Locate every uninfected red blood cell.
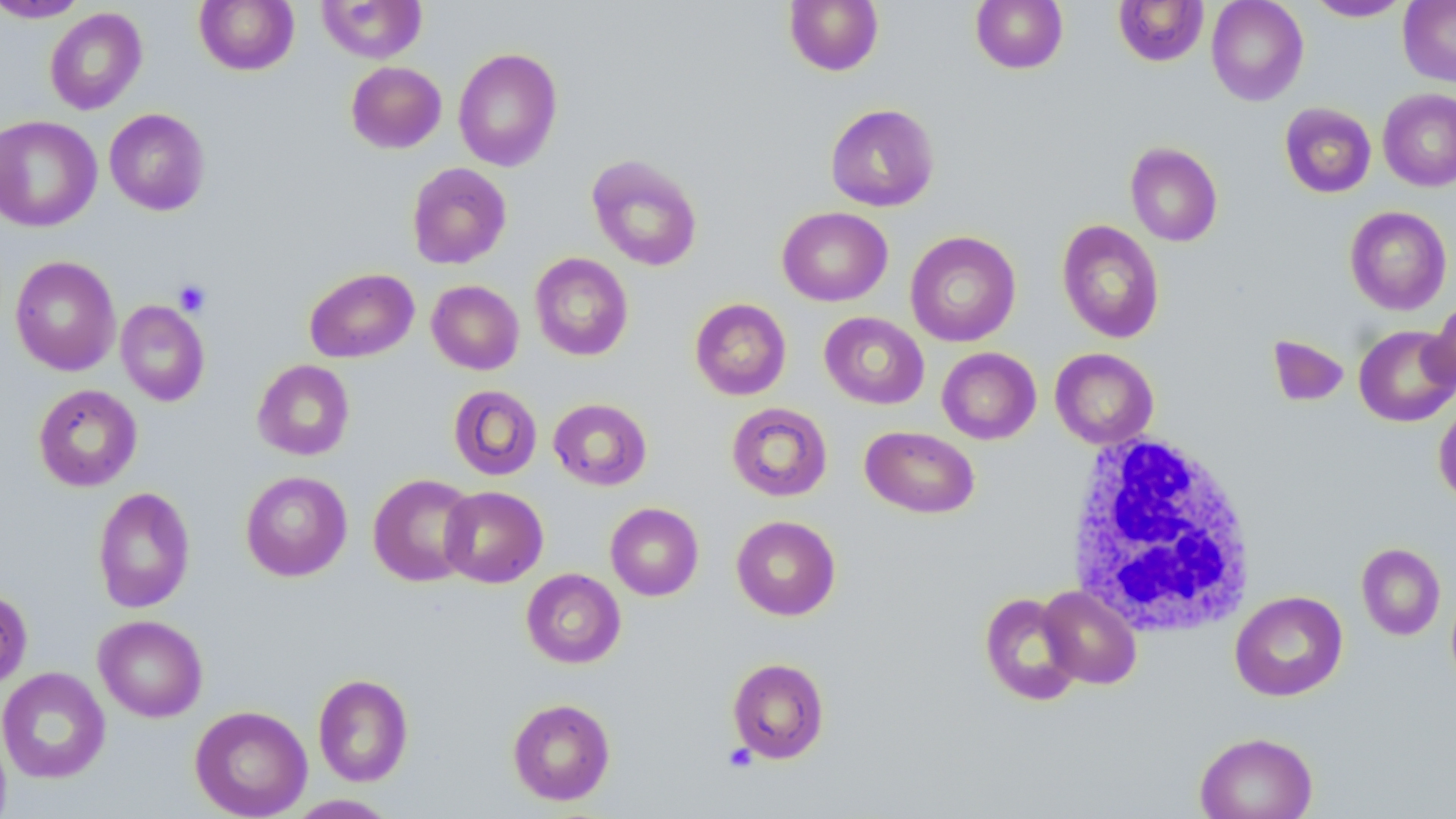
Approximate bounding boxes as (x1,y1)-(x2,y2) corner pairs in pixels.
Uninfected red blood cells: (0,0)-(90,23), (194,0)-(299,75), (783,0)-(884,76), (970,0)-(1068,74), (1113,0)-(1209,67), (1206,0)-(1309,106), (1304,0)-(1412,22), (316,1)-(427,63), (1399,1)-(1456,86), (44,7)-(148,115), (453,47)-(563,171), (345,61)-(447,153), (1378,88)-(1456,191), (1280,102)-(1376,198), (825,103)-(940,212), (104,108)-(211,215), (0,115)-(102,232), (1125,142)-(1223,246), (587,153)-(703,272), (406,162)-(512,269), (1344,205)-(1452,315), (777,206)-(892,306), (1057,220)-(1165,344), (905,231)-(1021,346), (530,253)-(633,361), (9,255)-(121,376), (304,268)-(419,363), (427,280)-(524,375), (689,298)-(792,400), (116,299)-(210,406), (1424,300)-(1456,397), (819,312)-(929,409), (1353,324)-(1456,427), (1268,334)-(1454,410), (1268,335)-(1350,407), (937,347)-(1041,444), (1050,348)-(1158,449), (252,359)-(355,461), (32,384)-(143,491), (448,385)-(542,480), (548,398)-(652,491), (1433,400)-(1456,505), (726,402)-(833,502), (860,426)-(980,519), (240,471)-(352,581), (368,473)-(478,587), (439,485)-(548,588), (92,486)-(195,613), (605,502)-(703,600), (731,515)-(841,621), (1356,542)-(1446,640), (521,568)-(625,669), (1038,585)-(1142,689), (0,587)-(32,690), (1229,590)-(1348,701), (979,592)-(1083,706), (94,614)-(208,722), (727,657)-(830,763), (0,667)-(110,784), (313,673)-(413,787), (507,698)-(616,806), (189,705)-(312,818), (0,724)-(11,819), (1194,730)-(1318,819), (285,794)-(400,817).

Summary:
  - White blood cell locations: (1066,431)-(1258,636)
  - Platelet locations: (174,280)-(211,317), (723,743)-(757,773)
  - Slide-level diagnosis: no evidence of blood parasites
  - Modality: optical microscopy
  - Magnification: 1000x
  - Preparation: thin blood film
  - Field of view: one of a larger specimen
  - Stain: May-Grünwald-Giemsa
  - Image size: 1456×819 pixels